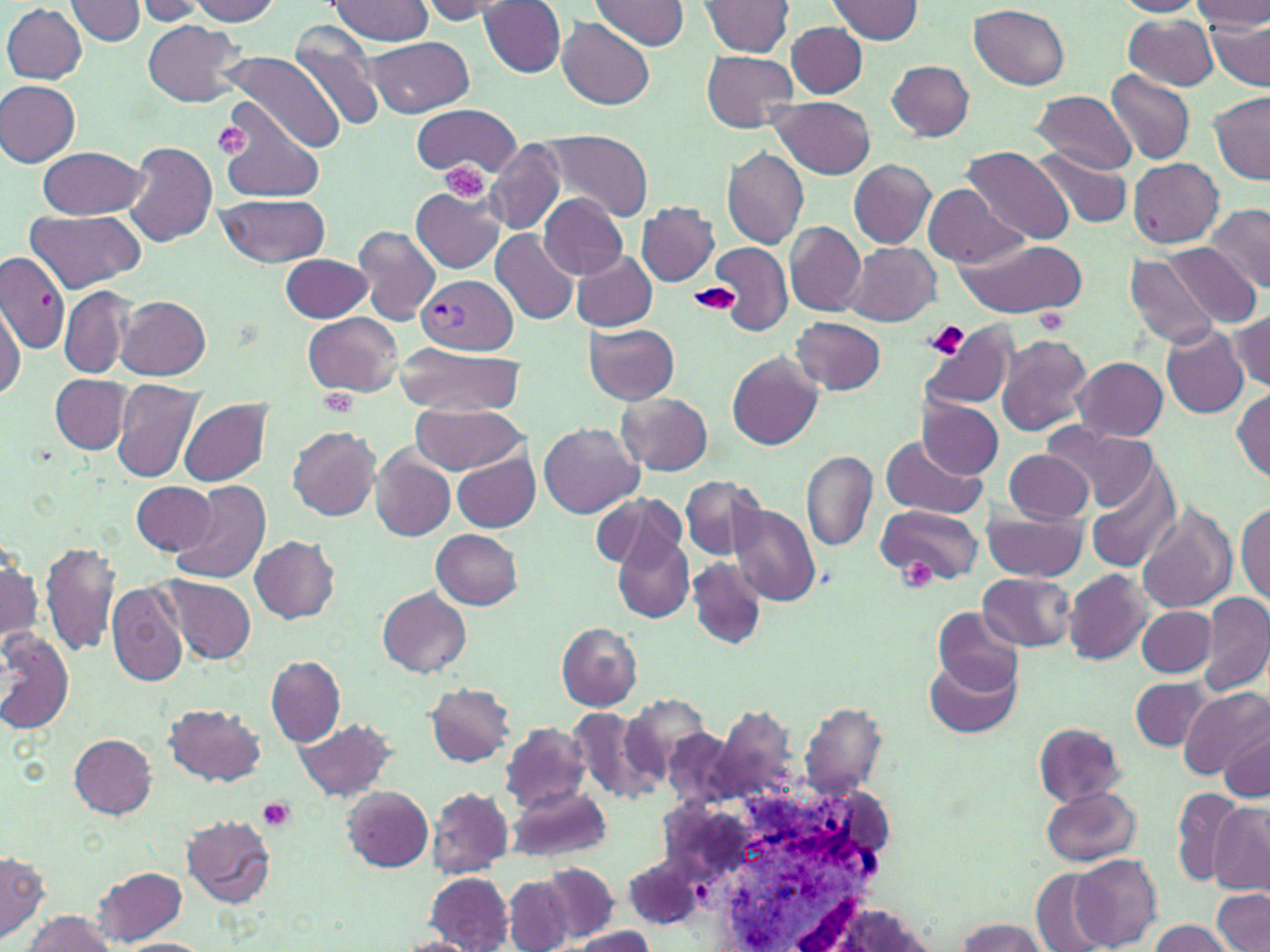

slide_level_diagnosis: Plasmodium vivax
modality: light microscopy
stain: May-Grünwald-Giemsa
preparation: thin blood film
plasmodium_vivax_infected_red_blood_cell_locations: 'approximate bounding boxes as [x1, y1, x2, y2] in pixels: [419, 273, 517, 355]'
platelet_locations: 'approximate bounding boxes as [x1, y1, x2, y2] in pixels: [213, 121, 252, 160], [439, 161, 489, 203], [687, 282, 741, 314], [1036, 309, 1068, 334], [925, 322, 969, 359], [318, 387, 359, 416], [899, 560, 937, 591], [257, 796, 295, 832]'
magnification: 1000x
image_size: 1270×952 pixels
white_blood_cell_locations: 'approximate bounding boxes as [x1, y1, x2, y2] in pixels: [632, 762, 908, 946]'
field_of_view: single
uninfected_red_blood_cell_locations: 'approximate bounding boxes as [x1, y1, x2, y2] in pixels: [187, 0, 283, 25], [329, 0, 433, 46], [420, 0, 521, 22], [589, 0, 691, 52], [700, 0, 794, 56], [828, 0, 924, 44], [1111, 0, 1204, 17], [1191, 0, 1270, 33], [67, 1, 145, 46], [134, 1, 207, 24], [479, 1, 567, 78], [2, 4, 86, 83], [970, 4, 1071, 89], [1123, 15, 1219, 90], [559, 18, 656, 110], [1206, 19, 1270, 89], [142, 20, 247, 108], [787, 21, 867, 98], [288, 25, 385, 132], [365, 36, 477, 116], [699, 50, 799, 133], [225, 51, 344, 155], [886, 60, 975, 141], [1106, 69, 1196, 165], [0, 80, 80, 167], [1029, 90, 1138, 175], [1209, 91, 1270, 183], [770, 96, 876, 179], [217, 99, 325, 202], [410, 105, 521, 177], [537, 129, 655, 222], [485, 139, 565, 233], [124, 142, 217, 248], [38, 145, 147, 220], [721, 147, 810, 249], [960, 147, 1076, 245], [1032, 150, 1133, 229], [1128, 157, 1222, 248], [849, 159, 937, 249], [923, 183, 1026, 270], [409, 187, 506, 274], [217, 193, 329, 268], [537, 193, 628, 280], [636, 202, 719, 286], [1203, 202, 1269, 292], [23, 210, 143, 290], [784, 221, 867, 317], [353, 225, 440, 325], [489, 230, 578, 325], [955, 236, 1087, 318], [844, 242, 941, 327], [709, 243, 792, 333], [1166, 245, 1263, 328], [571, 252, 658, 332], [0, 253, 69, 355], [278, 253, 373, 322], [1125, 254, 1220, 349], [58, 286, 133, 379], [116, 295, 211, 380], [0, 302, 24, 402], [1231, 310, 1270, 390], [302, 312, 403, 397], [789, 317, 885, 395], [920, 322, 1018, 411], [584, 323, 679, 404], [1159, 325, 1249, 418], [995, 333, 1093, 437], [395, 344, 523, 417], [726, 354, 822, 450], [1073, 357, 1168, 444], [51, 375, 130, 452], [111, 377, 205, 483], [1232, 387, 1270, 482], [618, 392, 713, 476], [917, 397, 1005, 478], [178, 399, 274, 488], [410, 402, 524, 474], [538, 422, 643, 517], [1047, 424, 1158, 512], [287, 425, 381, 521], [878, 435, 986, 519], [451, 448, 541, 533], [370, 449, 456, 541], [1004, 449, 1092, 525], [802, 451, 877, 551], [1089, 465, 1182, 575], [679, 475, 764, 560], [169, 480, 272, 585], [131, 481, 218, 555], [591, 492, 684, 574], [1235, 500, 1269, 605], [727, 503, 820, 607], [875, 503, 983, 585], [1136, 503, 1236, 613], [982, 508, 1087, 580], [431, 529, 524, 610], [612, 530, 693, 623], [250, 535, 340, 623], [41, 540, 119, 656], [1, 552, 41, 644], [686, 556, 767, 650], [1064, 569, 1152, 664], [978, 572, 1076, 651], [159, 574, 256, 665], [105, 583, 189, 688], [376, 587, 471, 677], [1198, 595, 1269, 694], [1136, 606, 1217, 676], [933, 607, 1023, 697], [555, 622, 642, 711], [0, 628, 74, 735], [265, 654, 346, 746], [924, 654, 1021, 739], [1132, 677, 1210, 751], [426, 684, 513, 767], [1177, 687, 1270, 780], [620, 696, 711, 787], [800, 700, 886, 798], [166, 703, 265, 784], [566, 704, 656, 800], [294, 717, 398, 800], [498, 721, 593, 810], [1033, 722, 1129, 806], [1219, 726, 1269, 801], [69, 734, 157, 819], [508, 783, 612, 864], [1040, 784, 1142, 865], [341, 786, 434, 872], [427, 787, 513, 879], [1170, 787, 1249, 886], [1209, 805, 1270, 893], [181, 814, 277, 908], [1, 852, 49, 944], [1070, 854, 1163, 950], [539, 863, 620, 942], [93, 866, 185, 945], [1031, 870, 1111, 950], [424, 871, 514, 950], [503, 875, 575, 952], [1211, 888, 1270, 952], [798, 900, 943, 951], [562, 908, 654, 943], [21, 910, 117, 952], [952, 917, 1050, 951], [1145, 919, 1235, 952], [568, 926, 658, 951], [391, 935, 475, 952], [119, 939, 211, 952]'